Locate every blood parasite and identify its species.
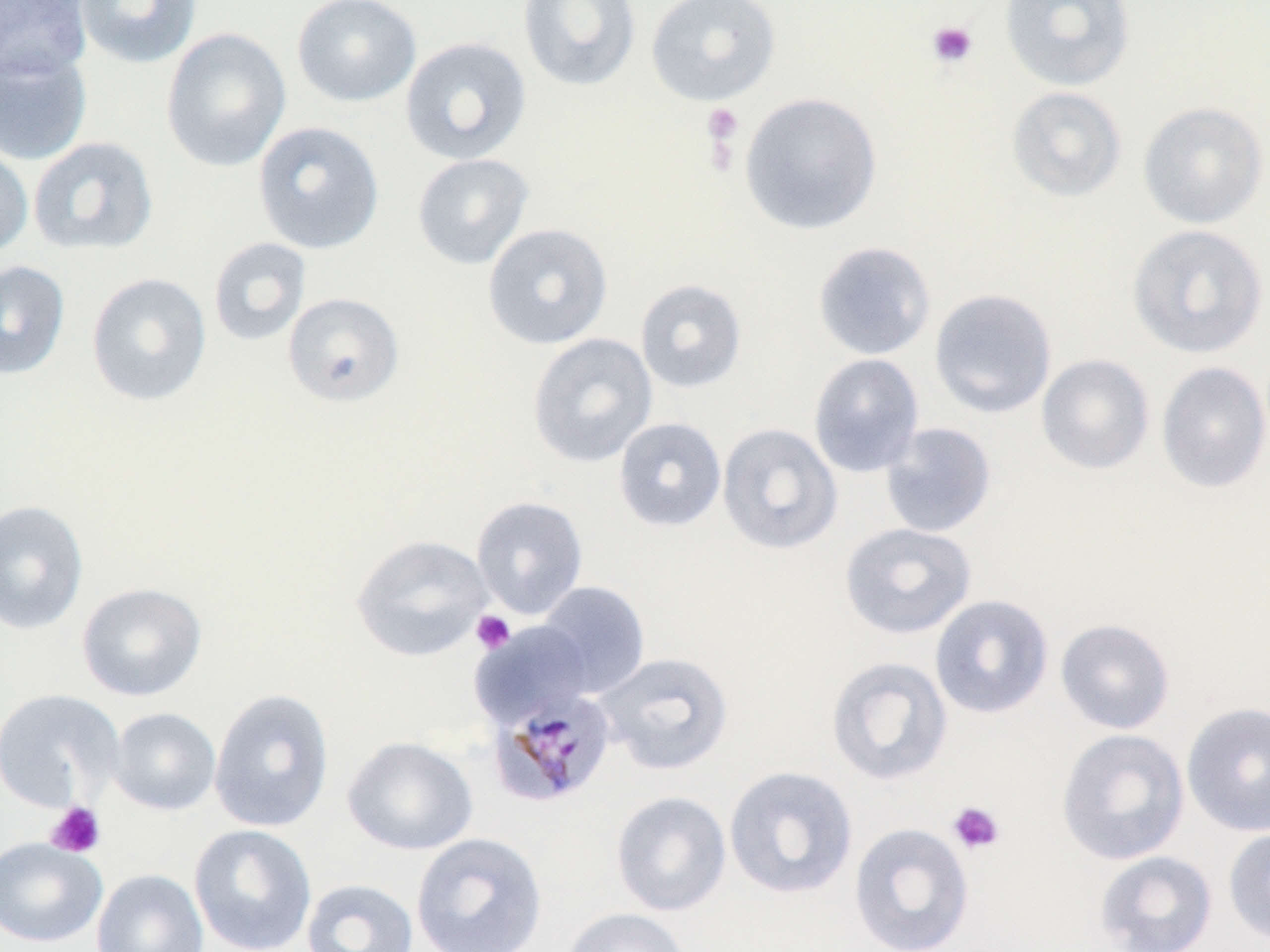
Approximate bounding boxes as named x1/y1/x2/y2 corners in pixels.
Plasmodium malariae-infected red blood cells: (x1=488, y1=686, x2=620, y2=809).
No Plasmodium falciparum, Plasmodium ovale, Plasmodium vivax, Babesia divergens, or Trypanosoma brucei observed.

Uninfected red blood cell locations: (x1=0, y1=0, x2=91, y2=81), (x1=74, y1=0, x2=202, y2=69), (x1=291, y1=0, x2=421, y2=107), (x1=517, y1=0, x2=642, y2=92), (x1=645, y1=0, x2=781, y2=106), (x1=999, y1=0, x2=1135, y2=92), (x1=161, y1=27, x2=291, y2=172), (x1=400, y1=36, x2=532, y2=165), (x1=0, y1=46, x2=92, y2=166), (x1=1007, y1=86, x2=1127, y2=203), (x1=739, y1=92, x2=883, y2=235), (x1=1138, y1=102, x2=1268, y2=228), (x1=252, y1=121, x2=385, y2=254), (x1=28, y1=136, x2=159, y2=256), (x1=0, y1=138, x2=34, y2=259), (x1=412, y1=152, x2=534, y2=269), (x1=482, y1=222, x2=613, y2=349), (x1=1127, y1=224, x2=1269, y2=358), (x1=208, y1=237, x2=312, y2=347), (x1=812, y1=240, x2=937, y2=361), (x1=0, y1=260, x2=70, y2=380), (x1=85, y1=272, x2=212, y2=406), (x1=635, y1=279, x2=747, y2=393), (x1=929, y1=288, x2=1057, y2=419), (x1=282, y1=292, x2=405, y2=407), (x1=527, y1=333, x2=658, y2=467), (x1=808, y1=353, x2=925, y2=478), (x1=1036, y1=354, x2=1155, y2=475), (x1=1156, y1=361, x2=1270, y2=493), (x1=613, y1=417, x2=727, y2=532), (x1=717, y1=422, x2=843, y2=555), (x1=879, y1=422, x2=998, y2=538), (x1=471, y1=496, x2=588, y2=619), (x1=0, y1=499, x2=89, y2=635), (x1=839, y1=522, x2=978, y2=640), (x1=351, y1=534, x2=493, y2=662), (x1=536, y1=581, x2=650, y2=698), (x1=76, y1=582, x2=208, y2=702), (x1=930, y1=594, x2=1054, y2=719), (x1=1055, y1=618, x2=1175, y2=734), (x1=472, y1=621, x2=595, y2=727), (x1=596, y1=651, x2=734, y2=775), (x1=825, y1=655, x2=953, y2=786), (x1=209, y1=687, x2=335, y2=832), (x1=0, y1=688, x2=124, y2=812), (x1=1181, y1=701, x2=1270, y2=837), (x1=108, y1=707, x2=222, y2=815), (x1=1056, y1=728, x2=1190, y2=865), (x1=342, y1=735, x2=479, y2=855), (x1=724, y1=765, x2=858, y2=899), (x1=610, y1=790, x2=731, y2=917), (x1=848, y1=822, x2=975, y2=952), (x1=189, y1=824, x2=317, y2=952), (x1=1223, y1=825, x2=1270, y2=946), (x1=411, y1=832, x2=548, y2=952), (x1=0, y1=836, x2=107, y2=947), (x1=1093, y1=850, x2=1218, y2=952), (x1=91, y1=868, x2=209, y2=952), (x1=301, y1=878, x2=419, y2=952), (x1=562, y1=907, x2=691, y2=952). Platelet locations: (x1=926, y1=20, x2=978, y2=68), (x1=702, y1=102, x2=744, y2=150), (x1=470, y1=610, x2=516, y2=654), (x1=947, y1=800, x2=1006, y2=855), (x1=45, y1=801, x2=105, y2=858). Slide-level diagnosis: Plasmodium malariae. Light microscopy. 1000x magnification. Single field of view. Thin blood smear. Image is 1270×952 pixels. May-Grünwald-Giemsa-stained preparation.